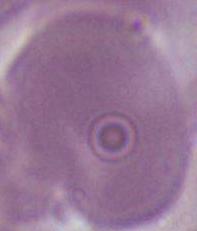

1000x magnification. An erythrocyte is shown. Photomicrograph.